Outline each Plasmodium vivax-infected red blood cell.
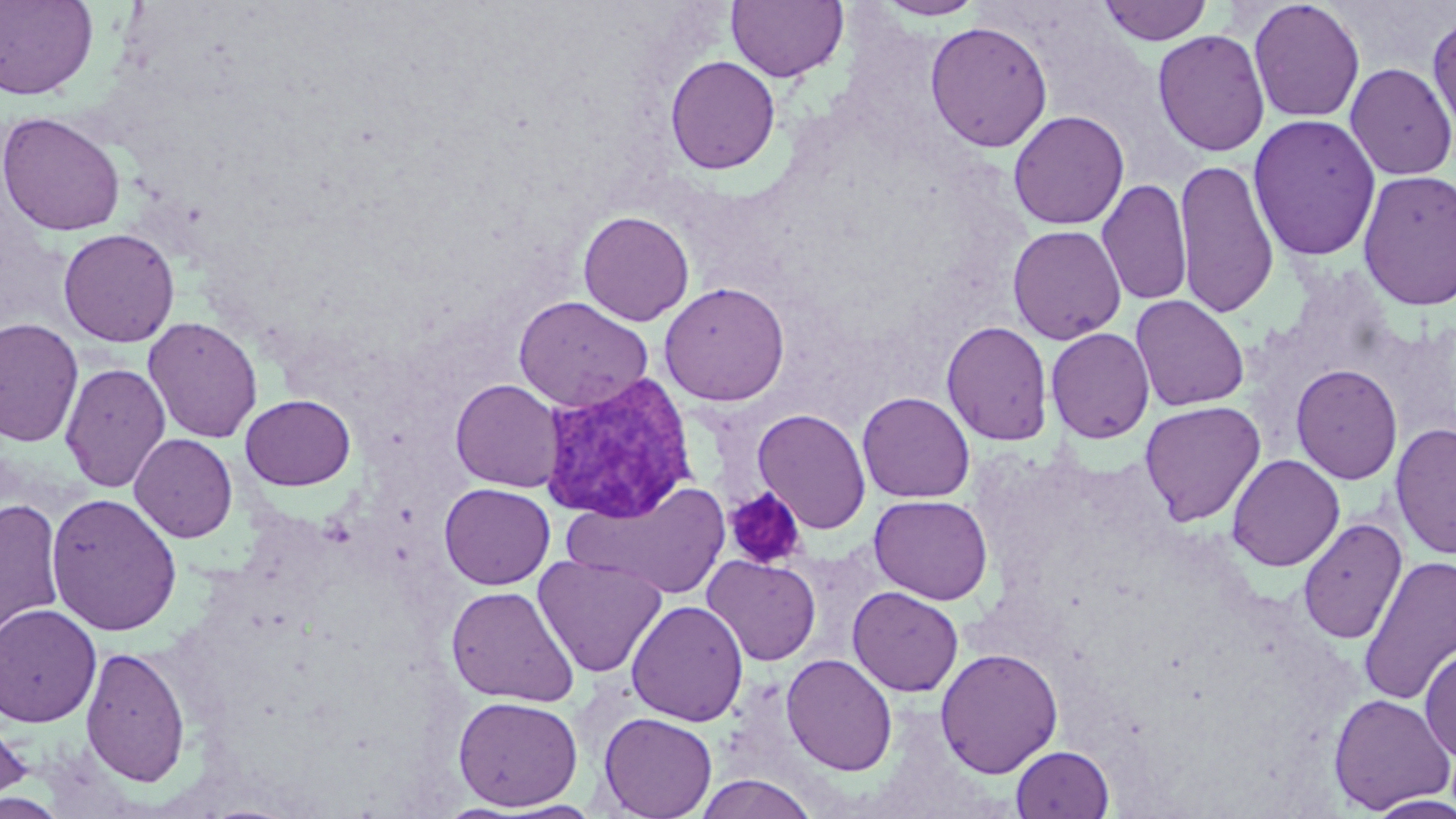

Approximate bounding boxes as [x1, y1, x2, y2] in pixels.
Plasmodium vivax-infected red blood cells: [540, 372, 697, 524].

Summary:
  - Uninfected red blood cell locations: [0, 0, 98, 101], [874, 0, 987, 20], [727, 1, 848, 83], [1097, 1, 1214, 46], [1248, 1, 1365, 122], [1427, 11, 1456, 142], [924, 21, 1053, 152], [1152, 29, 1270, 157], [664, 55, 781, 175], [1345, 62, 1456, 180], [1008, 110, 1130, 230], [0, 111, 125, 237], [1247, 114, 1382, 261], [1174, 158, 1279, 318], [1357, 169, 1456, 311], [1096, 178, 1193, 306], [578, 210, 694, 326], [1007, 225, 1127, 345], [58, 227, 180, 347], [659, 281, 790, 406], [1130, 294, 1250, 412], [513, 295, 653, 412], [142, 316, 263, 443], [0, 318, 84, 447], [941, 321, 1054, 446], [1046, 327, 1155, 443], [59, 362, 171, 492], [1290, 363, 1403, 485], [450, 378, 564, 492], [857, 391, 975, 503], [241, 393, 356, 491], [1139, 400, 1266, 526], [752, 408, 871, 535], [1390, 422, 1456, 560], [129, 434, 238, 542], [1226, 453, 1344, 571], [564, 481, 729, 599], [439, 483, 555, 589], [45, 492, 183, 637], [868, 494, 993, 604], [1, 497, 66, 643], [1297, 517, 1407, 645], [533, 554, 667, 678], [702, 555, 821, 666], [1358, 555, 1456, 706], [445, 585, 579, 706], [847, 586, 963, 697], [626, 600, 749, 727], [0, 603, 101, 727], [1420, 643, 1456, 764], [80, 646, 191, 787], [935, 647, 1063, 778], [781, 653, 898, 775], [1327, 693, 1454, 814], [453, 696, 583, 811], [0, 711, 34, 807], [598, 712, 718, 819], [1011, 745, 1114, 819], [693, 774, 818, 818], [0, 793, 68, 819], [1365, 794, 1456, 818], [494, 800, 607, 818]
  - Platelet locations: [724, 487, 808, 570]
  - Slide-level diagnosis: Plasmodium vivax
  - Stain: May-Grünwald-Giemsa
  - Magnification: 1000x
  - Image size: 1456×819 pixels
  - Preparation: thin blood smear
  - Modality: optical microscopy
  - Field of view: one of a larger specimen